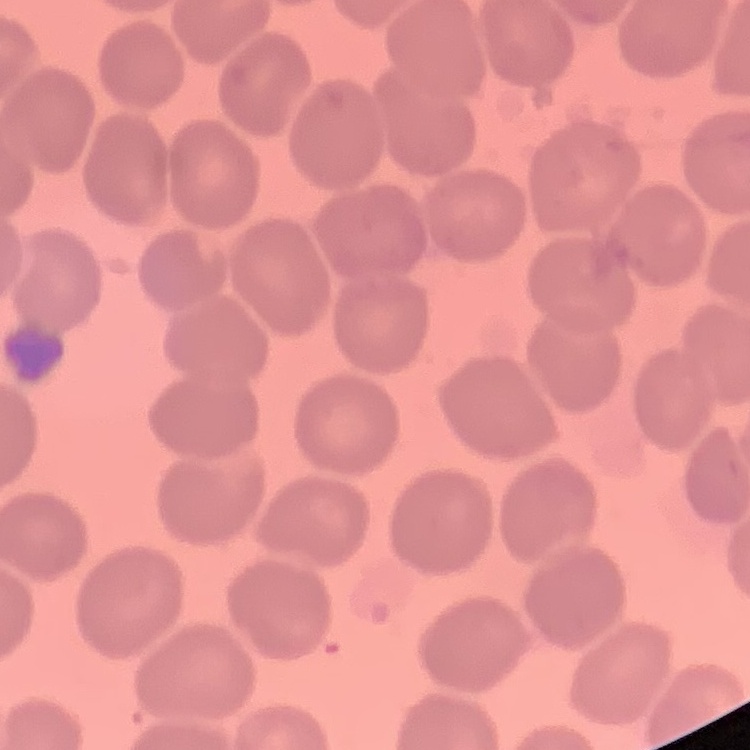 The red blood cells exhibit no rouleaux formation. Stained with either Field's or Giemsa. One tile cut from a larger photomicrograph. Thin blood film.